Classify this cell by malaria status.
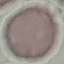
Uninfected.

Cell patch, automatically extracted from a larger field of view and resized to 64 × 64 pixels. Giemsa stain. Thin smear of blood. Acquired by smartphone through the microscope eyepiece.